Identify the preparation type.
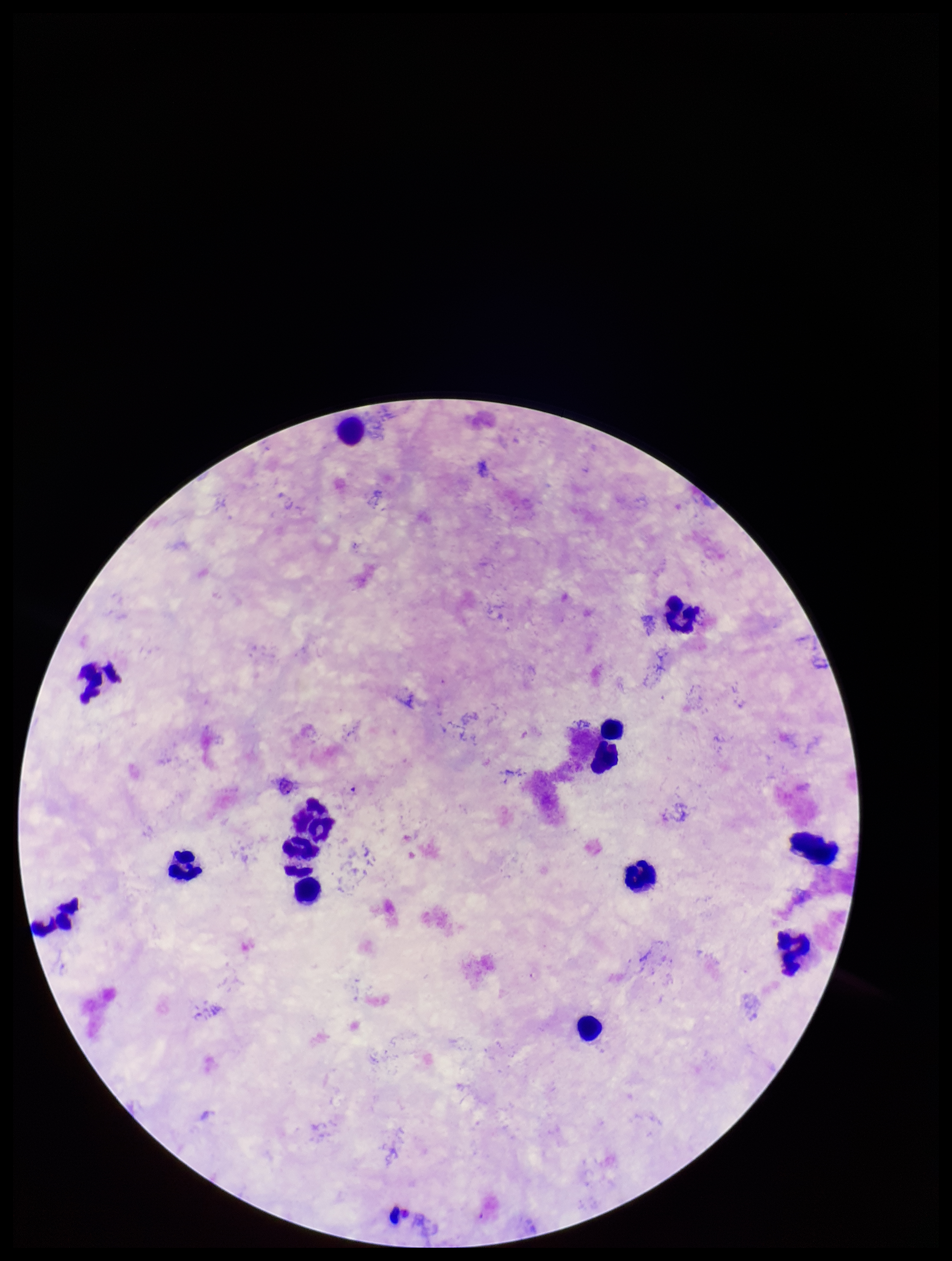

A thick smear.

stain = Giemsa
Plasmodium parasites = none seen
patient malaria status = negative
leukocyte count = 14
parasite count = 0
field of view = single
capture = smartphone photograph through the microscope eyepiece
image size = 952×1261 pixels